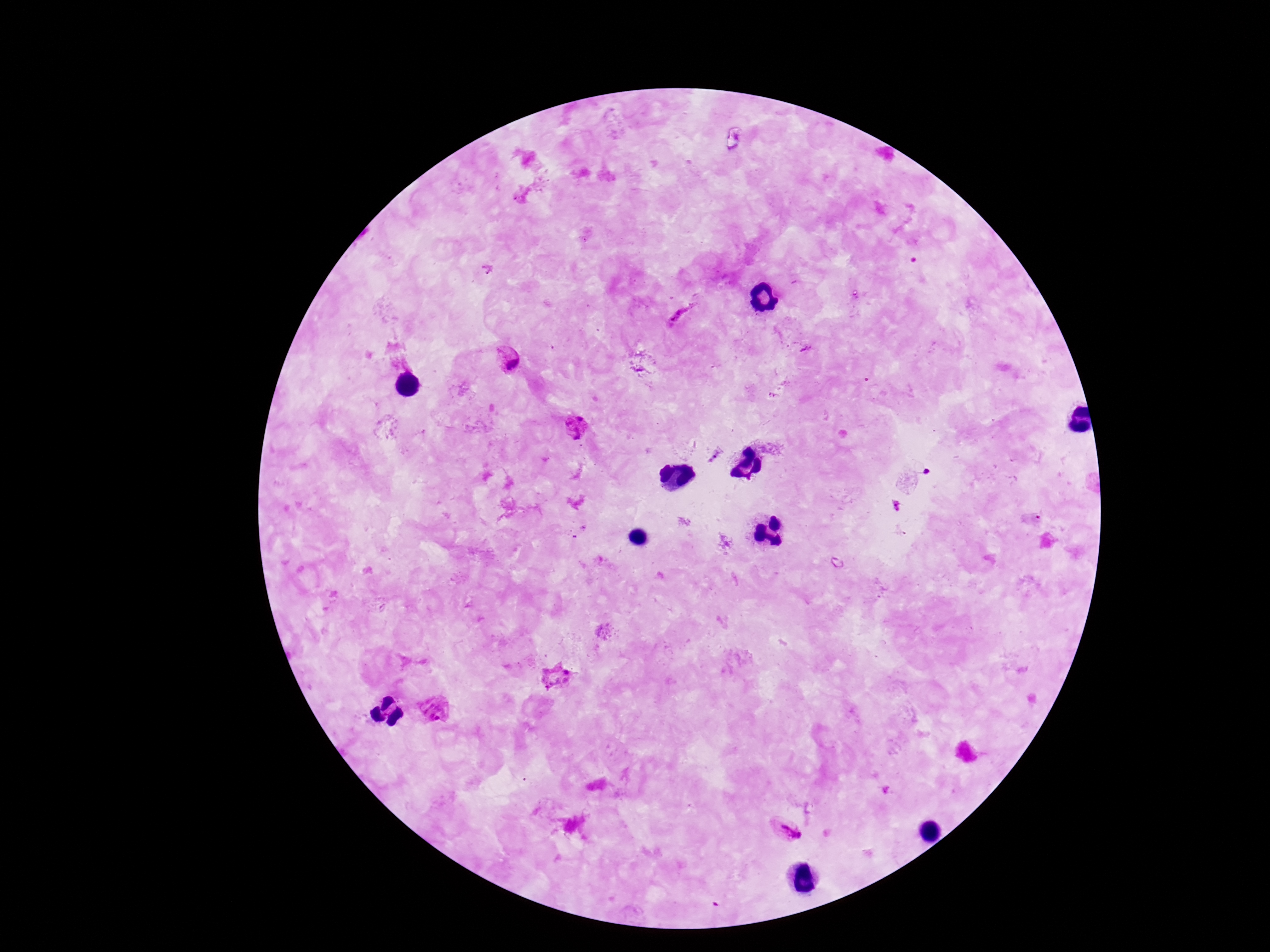

magnification = 100x
patient malaria status = positive
field of view = one from this slide
stain = Giemsa
Plasmodium parasite locations = approximate object centers, in pixels from the top-left corner: (x=487, y=269), (x=680, y=316), (x=806, y=349), (x=508, y=361), (x=639, y=367), (x=576, y=427), (x=714, y=457), (x=896, y=506), (x=557, y=675), (x=785, y=830)
image size = 1270×952 pixels
preparation = thick blood film
capture = smartphone camera through the microscope eyepiece